Assess this cell for malaria.
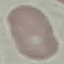

It is uninfected.

Thin blood smear. Acquired by smartphone through the microscope eyepiece. Giemsa stain. Cell patch, automatically extracted from a larger field of view and resized to 64 × 64 pixels.